Classify this cell by malaria status.
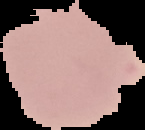

It is uninfected.

Cell region segmented out of the field of view; the surrounding area is masked to black. Image is 145×130 pixels. From a thin blood smear.